Classify the preparation.
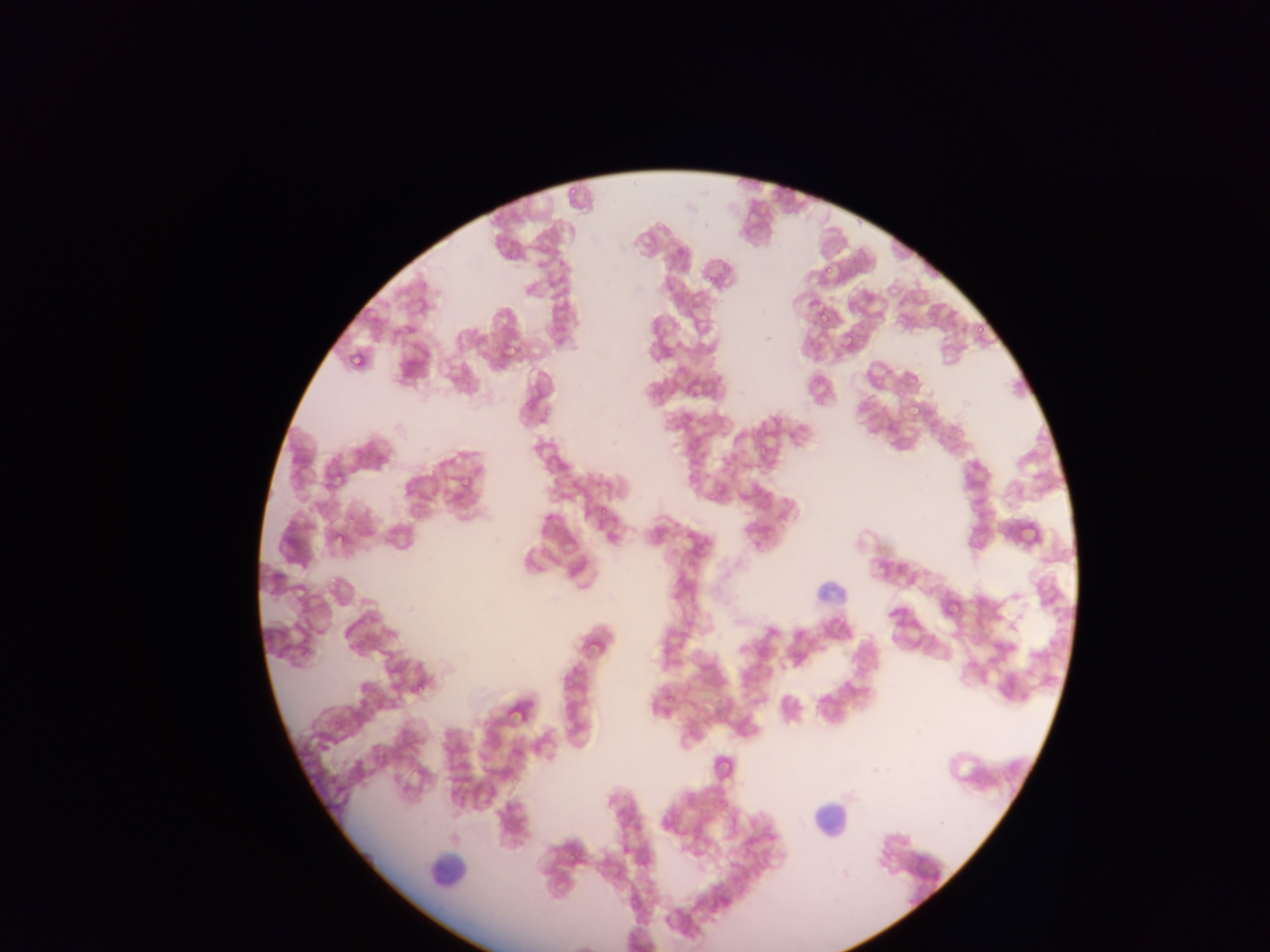
This is a thin smear.

Approximate bounding boxes as (left, top, right, bottom) in pixels.
Summary:
  - Plasmodium parasite locations: (568, 185, 578, 194), (825, 266, 834, 276), (703, 271, 719, 284), (819, 313, 832, 327), (958, 322, 969, 336), (977, 326, 986, 337), (840, 335, 854, 350), (977, 335, 985, 342), (347, 348, 364, 365), (908, 406, 922, 418), (461, 477, 472, 490), (712, 481, 728, 493), (600, 508, 608, 514), (334, 534, 347, 545), (792, 648, 804, 657), (416, 685, 426, 694), (667, 694, 676, 702)
  - Leukocyte locations: (814, 570, 862, 613), (812, 788, 846, 847), (420, 841, 481, 895)
  - Capture: mobile-phone photograph through a microscope
  - Country: Ghana
  - Image size: 1270×952 pixels
  - Field of view: single